Locate every blood parasite and identify its species.
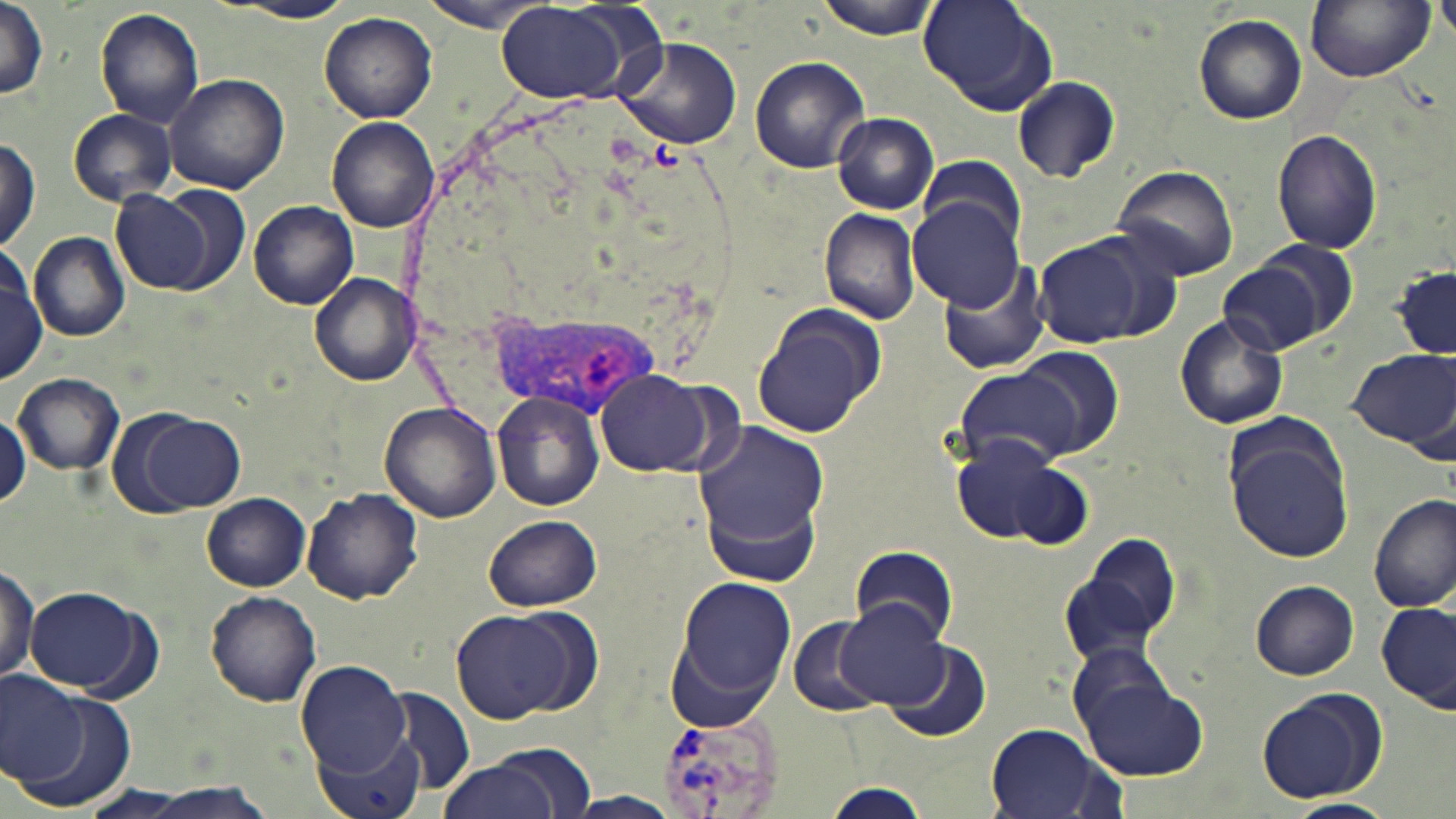
Approximate bounding boxes as (x1,y1)-(x2,y2) corner pairs in pixels.
Plasmodium vivax-infected red blood cells: (493,310)-(664,419), (656,712)-(786,819).
No Plasmodium falciparum, Plasmodium ovale, Plasmodium malariae, Babesia divergens, or Trypanosoma brucei observed.

{
  "slide_level_diagnosis": "Plasmodium vivax",
  "field_of_view": "single",
  "preparation": "thin blood smear",
  "modality": "optical microscopy",
  "magnification": "1000x",
  "image_size": "1456×819 pixels",
  "uninfected_red_blood_cell_locations": "approximate bounding boxes as (x1,y1)-(x2,y2) corner pairs in pixels: (817,0)-(946,39), (919,0)-(1057,118), (1436,0)-(1456,43), (421,1)-(552,33), (1306,1)-(1433,83), (219,2)-(360,23), (0,3)-(49,100), (496,3)-(631,102), (95,8)-(206,128), (320,11)-(438,123), (1192,13)-(1308,125), (615,37)-(743,149), (748,56)-(870,174), (165,72)-(290,194), (1011,75)-(1121,183), (67,109)-(177,206), (832,112)-(939,214), (327,117)-(439,232), (1271,130)-(1383,254), (1,139)-(41,255), (918,154)-(1025,253), (1111,165)-(1240,282), (159,185)-(253,294), (113,188)-(219,294), (909,197)-(1027,312), (248,200)-(359,309), (819,207)-(920,325), (29,233)-(131,342), (1034,236)-(1150,346), (1250,242)-(1358,344), (0,253)-(47,384), (939,262)-(1052,376), (1218,262)-(1323,356), (1393,266)-(1454,359), (310,273)-(421,385), (750,306)-(882,437), (1174,314)-(1288,429), (1016,346)-(1125,455), (1345,348)-(1454,449), (954,363)-(1084,469), (596,370)-(715,474), (12,371)-(124,474), (493,390)-(606,511), (380,400)-(502,522), (0,413)-(26,502), (135,413)-(246,511), (692,423)-(835,555), (1222,424)-(1354,564), (951,434)-(1066,543), (1011,464)-(1094,550), (702,480)-(824,590), (301,487)-(422,604), (203,492)-(309,592), (1370,493)-(1454,613), (484,514)-(602,612), (1063,533)-(1182,665), (850,547)-(959,644), (0,561)-(39,688), (670,572)-(797,717), (1250,580)-(1360,679), (26,585)-(153,697), (207,591)-(321,706), (834,598)-(956,708), (1378,600)-(1455,712), (449,607)-(588,724), (788,616)-(888,717), (881,640)-(991,743), (1062,642)-(1181,744), (297,661)-(411,780), (1,673)-(87,785), (1078,678)-(1207,781), (3,683)-(140,816), (385,685)-(474,797), (1253,687)-(1384,803), (985,725)-(1115,819), (313,730)-(426,819), (437,759)-(563,819), (819,781)-(934,818), (563,793)-(681,817), (1282,798)-(1395,819)",
  "stain": "May-Grünwald-Giemsa"
}